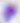
400x magnification. Toxoplasma gondii is seen. Micrograph.